Identify the blood parasite species.
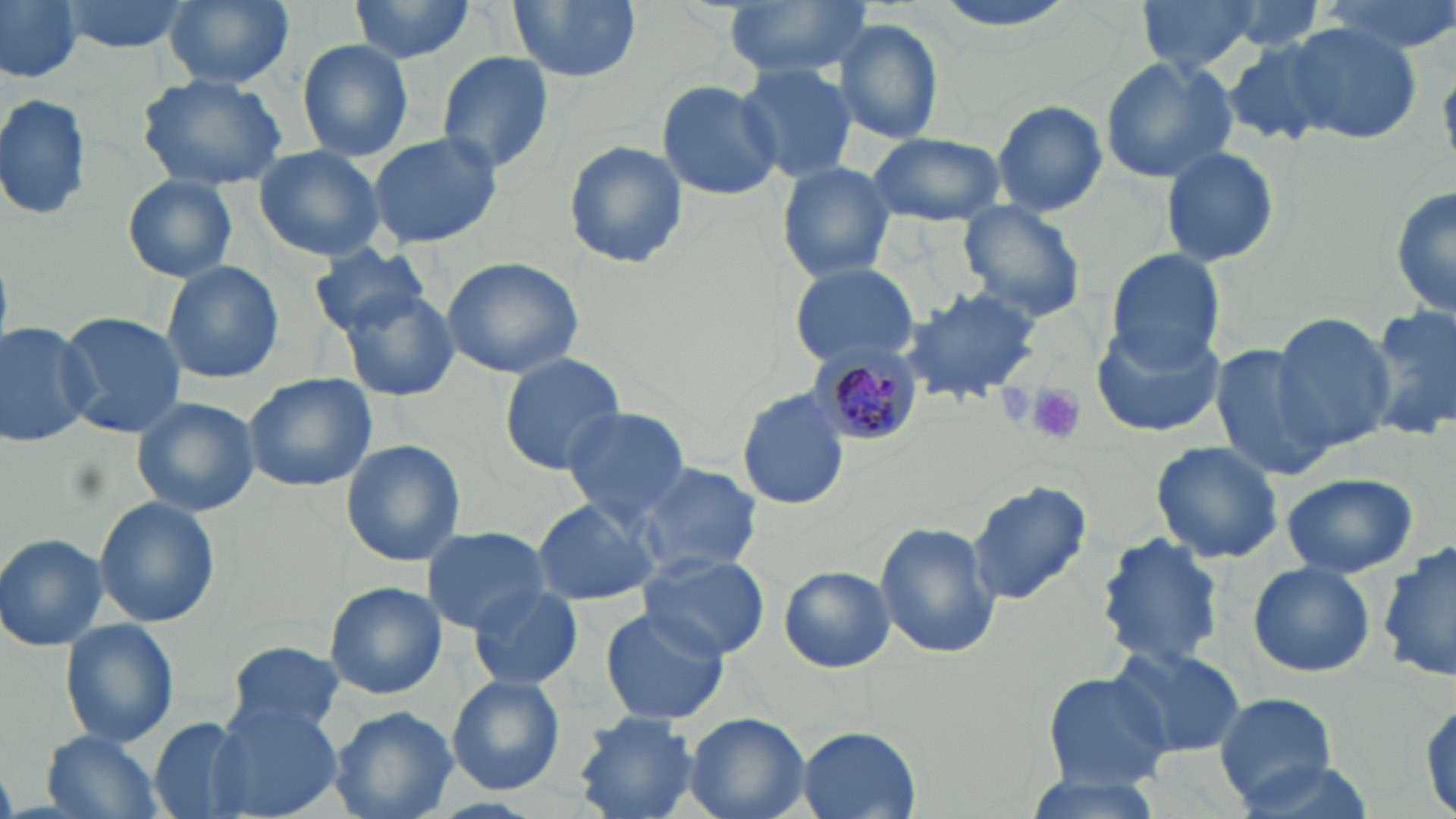
Plasmodium malariae.

magnification = 1000x
field of view = one of a larger specimen
stain = May-Grünwald-Giemsa
preparation = thin blood film
modality = light microscopy
uninfected red blood cell locations = approximate bounding boxes as [x1, y1, x2, y2] in pixels: [0, 0, 156, 74], [0, 0, 84, 85], [59, 0, 191, 53], [162, 0, 294, 90], [350, 0, 480, 64], [508, 0, 640, 84], [724, 0, 870, 79], [925, 0, 1085, 32], [1135, 0, 1264, 74], [1319, 0, 1453, 55], [833, 19, 946, 145], [1282, 22, 1422, 143], [1221, 39, 1339, 147], [296, 40, 414, 162], [437, 52, 555, 173], [1099, 54, 1238, 184], [734, 63, 858, 183], [138, 72, 288, 190], [658, 78, 778, 201], [0, 93, 92, 223], [991, 99, 1107, 216], [867, 130, 1007, 226], [367, 131, 502, 249], [562, 139, 689, 270], [1160, 144, 1281, 267], [254, 146, 384, 260], [776, 160, 896, 281], [120, 175, 238, 284], [1391, 175, 1456, 324], [955, 200, 1088, 324], [309, 243, 433, 338], [1105, 250, 1226, 367], [440, 257, 585, 379], [161, 261, 285, 385], [787, 261, 920, 369], [898, 286, 1045, 404], [340, 290, 462, 402], [1363, 304, 1456, 439], [57, 311, 186, 437], [1268, 313, 1395, 452], [1091, 320, 1228, 437], [0, 321, 96, 449], [1210, 345, 1331, 482], [498, 354, 627, 474], [243, 373, 377, 493], [736, 389, 849, 512], [133, 398, 260, 515], [560, 405, 693, 522], [340, 439, 467, 568], [1151, 441, 1284, 565], [631, 462, 763, 576], [1280, 472, 1419, 579], [967, 480, 1094, 606], [94, 498, 220, 626], [531, 499, 660, 607], [876, 522, 1000, 659], [421, 525, 551, 634], [1096, 533, 1227, 669], [1, 534, 107, 650], [1380, 542, 1455, 686], [636, 552, 769, 661], [1247, 561, 1378, 680], [779, 565, 895, 674], [323, 581, 448, 700], [468, 584, 583, 690], [597, 607, 729, 726], [59, 618, 178, 751], [224, 638, 346, 741], [1109, 644, 1246, 757], [1041, 669, 1172, 788], [446, 674, 565, 794], [1213, 692, 1342, 807], [1418, 694, 1454, 818], [210, 703, 342, 818], [328, 706, 457, 819], [684, 712, 811, 819], [574, 713, 703, 818], [147, 718, 256, 819], [798, 727, 920, 818], [41, 731, 166, 819], [1227, 754, 1380, 819], [1014, 772, 1165, 819]
platelet locations = approximate bounding boxes as [x1, y1, x2, y2] in pixels: [1029, 383, 1086, 444]
image size = 1456×819 pixels
Plasmodium malariae-infected red blood cell locations = approximate bounding boxes as [x1, y1, x2, y2] in pixels: [818, 352, 921, 445]